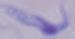

Summary:
  - Identification: trypanosome
  - Modality: micrograph
  - Magnification: 1000x